Outline every Plasmodium parasite.
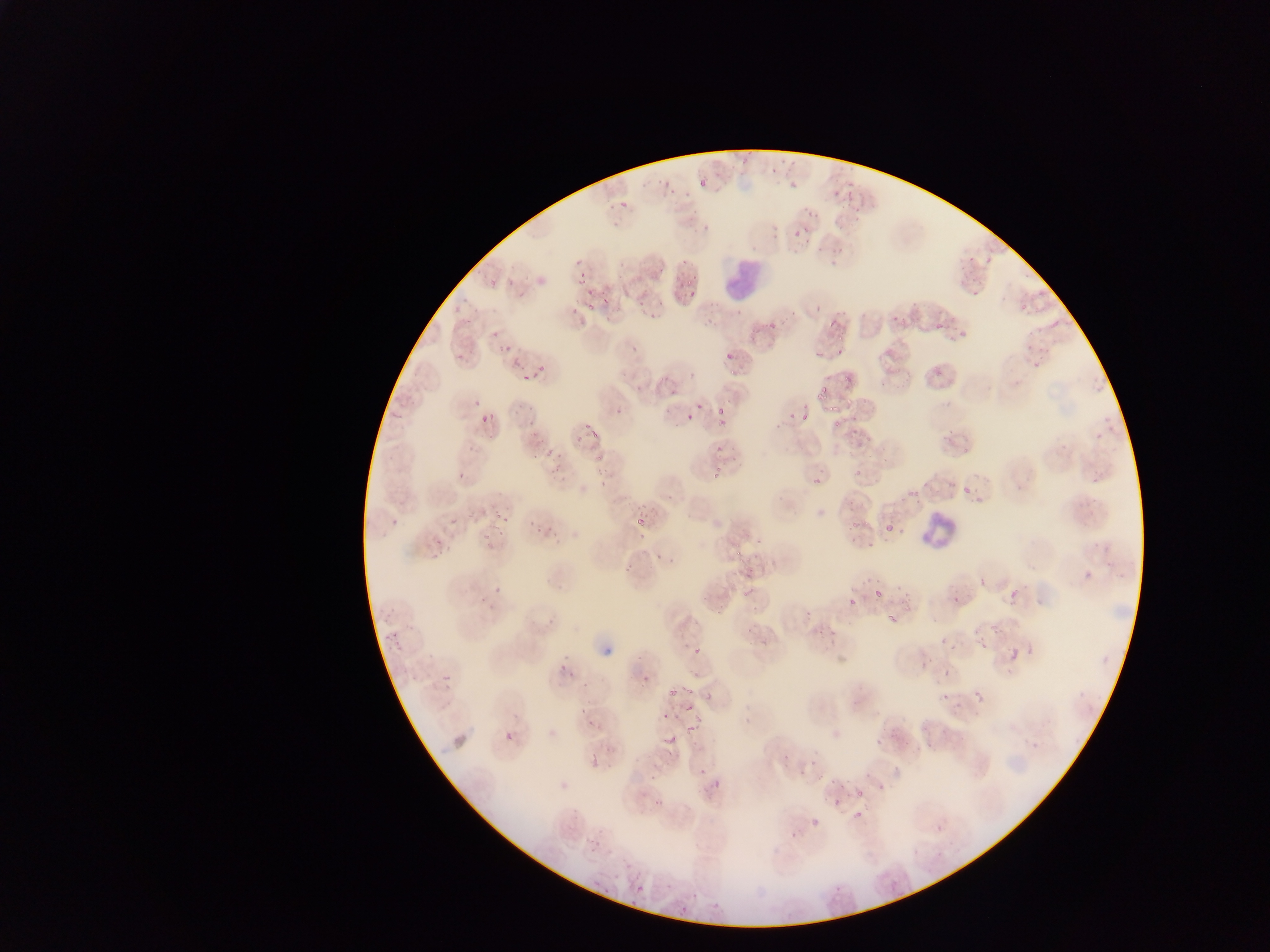
Approximate bounding boxes as left top right bottom in pixels.
Plasmodium parasites: 739 146 755 164; 770 163 779 175; 659 176 670 185; 846 177 853 192; 699 178 707 187; 788 181 800 192; 832 184 841 198; 665 186 678 196; 842 191 856 212; 619 196 635 207; 606 200 619 213; 803 201 821 220; 792 227 805 237; 830 236 847 262; 813 243 824 254; 966 250 975 264; 680 252 692 265; 572 256 585 266; 983 256 990 269; 618 261 628 270; 657 267 669 271; 577 273 587 285; 683 273 695 287; 505 277 516 288; 969 288 977 298; 583 291 594 299; 684 291 693 299; 601 292 615 316; 637 296 648 309; 587 301 599 311; 813 304 822 317; 568 306 575 315; 829 308 844 327; 645 309 660 319; 784 312 796 322; 463 313 471 322; 891 314 900 322; 1050 319 1060 328; 762 321 777 338; 935 323 943 330; 950 329 968 341; 491 332 499 339; 498 340 517 351; 628 345 639 356; 832 347 842 358; 1033 350 1049 371; 456 351 467 360; 812 353 820 361; 509 355 528 368; 724 356 733 359; 535 365 549 373; 686 367 695 380; 933 367 944 380; 876 369 891 389; 518 373 533 389; 635 382 645 396; 667 382 683 398; 816 382 838 403; 471 400 481 411; 693 401 705 412; 512 402 523 418; 820 402 839 413; 482 403 498 420; 612 405 627 417; 480 409 490 423; 661 409 676 415; 712 409 725 418; 718 409 730 430; 786 409 795 421; 802 411 808 420; 682 416 693 424; 850 416 860 421; 526 418 536 430; 584 420 592 431; 830 420 843 431; 776 422 781 430; 943 426 953 442; 851 428 861 437; 534 432 544 444; 589 432 603 443; 574 435 589 447; 962 442 971 457; 547 444 569 463; 466 446 475 453; 714 446 725 455; 531 450 542 459; 594 451 607 462; 546 466 559 477; 708 467 723 484; 855 469 862 478; 457 471 468 480; 1089 473 1101 485; 810 474 824 483; 596 479 605 488; 666 491 674 502; 492 503 510 524; 632 513 649 529; 385 516 399 529; 450 518 463 537; 527 519 535 533; 535 519 547 539; 846 519 859 533; 484 521 503 546; 885 525 894 535; 548 528 560 544; 638 529 647 541; 743 530 753 542; 430 535 448 561; 848 536 857 544; 756 540 765 547; 866 543 877 550; 734 548 743 556; 655 551 663 560; 670 554 687 563; 737 559 747 566; 1105 561 1113 569; 623 565 635 574; 1084 570 1093 580; 1113 571 1124 582; 744 572 756 580; 977 578 986 589; 873 579 881 588; 726 580 740 591; 491 584 502 599; 742 585 754 600; 1006 585 1023 608; 894 586 904 594; 873 589 882 600; 847 591 859 609; 477 592 488 606; 953 593 961 605; 900 594 913 605; 697 596 708 605; 381 598 398 624; 716 603 725 618; 490 605 500 613; 707 605 716 615; 804 610 813 619; 886 613 899 628; 989 619 1000 633; 745 626 755 635; 816 626 828 637; 830 629 840 640; 972 629 983 638; 383 634 402 649; 939 638 947 647; 981 643 988 651; 1025 644 1035 658; 694 646 702 655; 1009 649 1016 658; 920 657 932 667; 558 662 566 674; 568 669 576 682; 944 669 952 677; 439 670 450 687; 407 672 419 683; 642 673 649 683; 582 680 589 692; 679 681 694 697; 670 685 676 698; 973 689 987 707; 700 690 712 703; 941 693 949 700; 952 700 960 711; 679 702 693 717; 579 705 586 714; 662 713 667 721; 587 714 596 731; 682 721 700 736; 505 731 515 741; 870 733 888 750; 660 738 678 747; 899 738 912 748; 667 747 676 761; 782 750 794 762; 591 756 600 766; 696 768 705 777; 863 769 873 777; 799 772 805 780; 649 773 657 782; 815 773 824 784; 829 773 839 787; 711 781 721 793; 840 781 851 789; 876 783 883 794; 855 789 867 799; 639 790 646 800; 654 798 664 808; 831 798 841 808; 851 811 862 822; 809 819 820 829; 936 825 943 833; 788 830 797 838; 594 833 610 848; 613 873 623 882; 593 878 605 887; 889 879 896 888; 635 882 644 894; 663 883 671 891; 832 883 844 895; 601 888 609 896; 629 898 636 908; 678 909 688 915 | approximate x y pixel centers of objects too small to bound: 756 557; 811 764.

Leukocyte locations: 713 264 756 302; 913 497 973 563. Image is 1270×952 pixels. Collected in Ghana. Thin blood film. Photographed through a microscope with a mobile-phone camera. One field of view.